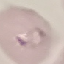

malaria status = parasitized
image type = cell patch, automatically extracted from a larger field of view and resized to 64 × 64 pixels
stain = Giemsa
preparation = thin blood film
capture = smartphone camera at the microscope eyepiece